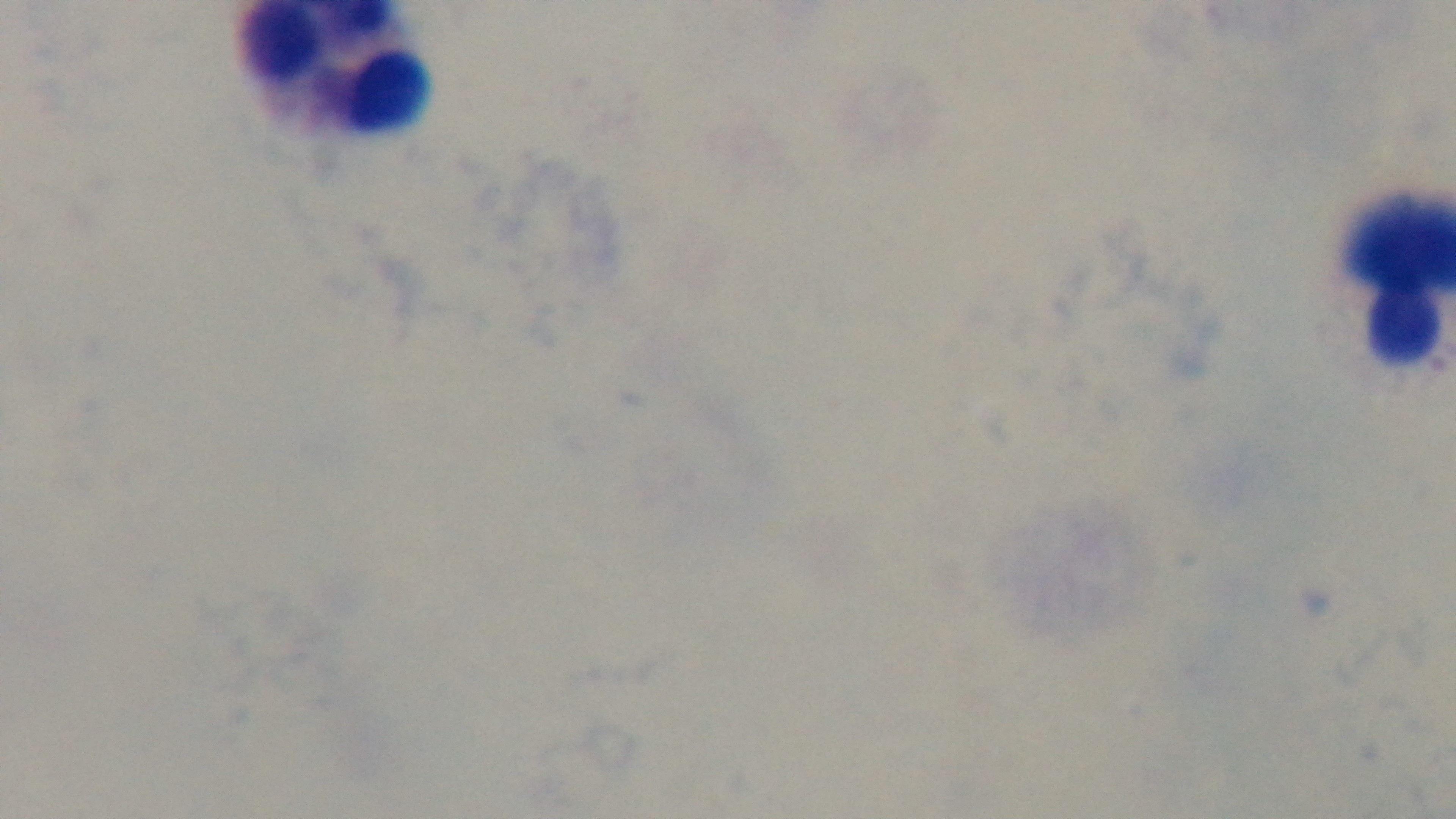

Summary:
  - Malaria status: uninfected
  - Field of view: single
  - Objective: 100x oil immersion
  - Preparation: thick blood film
  - Capture: mounted 4K digital camera
  - Modality: light microscopy
  - Stain: Giemsa